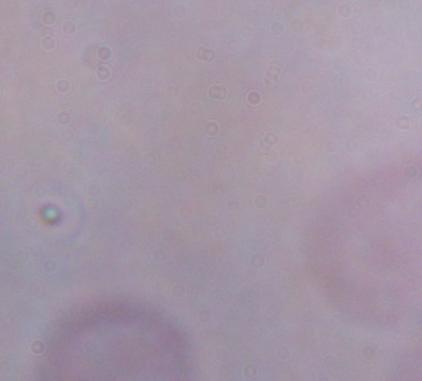
Summary:
  - Modality: photomicrograph
  - Identification: trypanosome
  - Magnification: 1000x